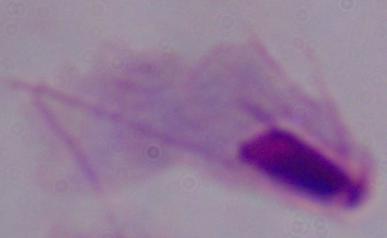
Summary:
  - Magnification: 1000x
  - Modality: photomicrograph
  - Identification: trichomonad